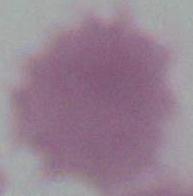 1000x magnification. Micrograph. A red blood cell is seen.